Assess this cell for malaria.
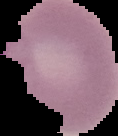

Parasitized.

Summary:
  - Preparation: thin blood smear
  - Image type: segmented cell region on a black background
  - Image size: 118×136 pixels